Give the position of every Plasmodium parasite and every leukocyte.
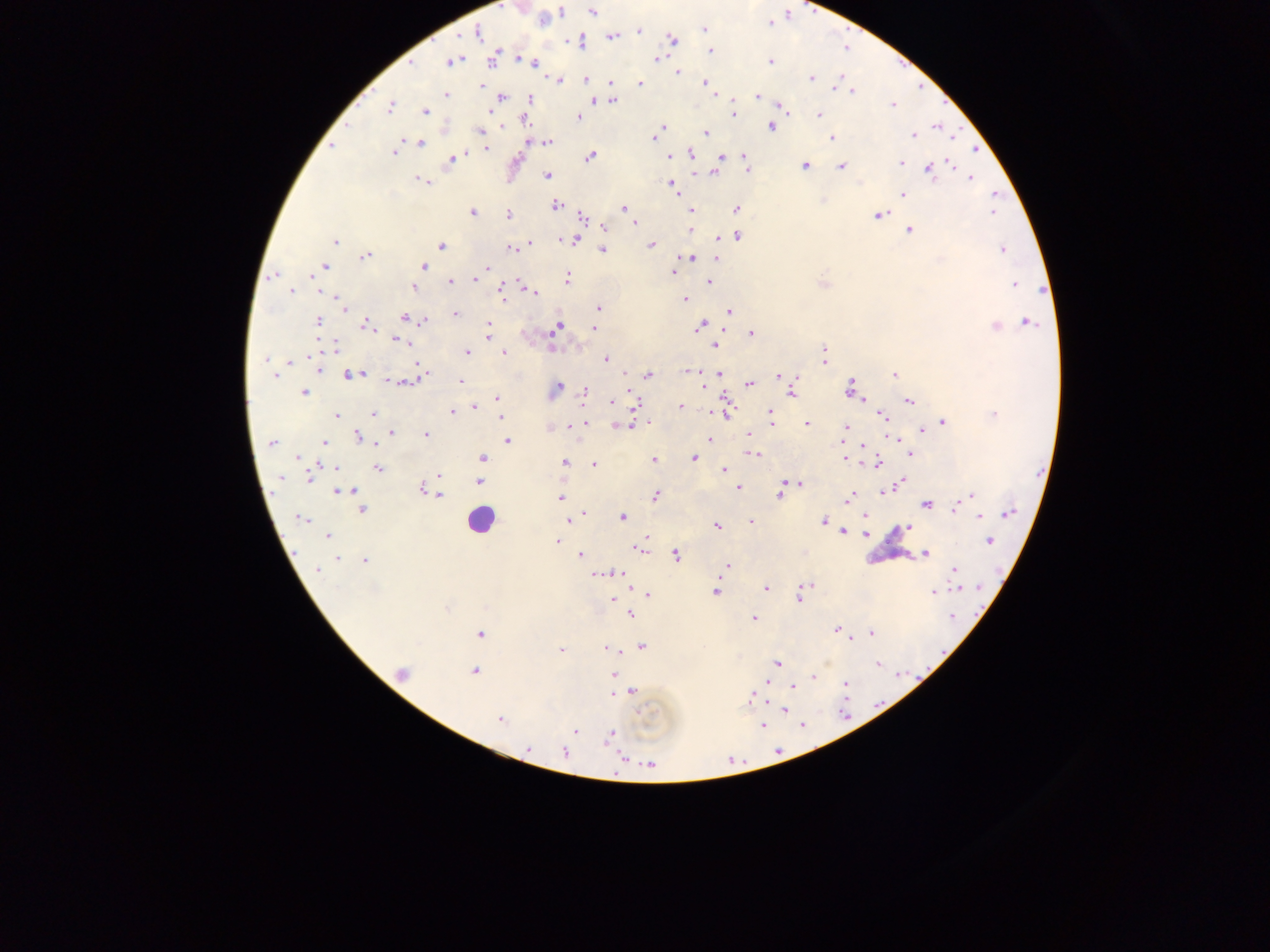
Approximate centers as x y in pixels.
Plasmodium parasites: 592 12; 543 19; 705 29; 639 31; 477 33; 612 37; 673 39; 579 42; 710 51; 492 59; 524 60; 657 60; 452 62; 532 62; 770 62; 677 73; 811 78; 586 79; 558 80; 611 82; 705 82; 640 83; 838 83; 481 85; 852 91; 446 95; 757 96; 502 97; 531 98; 594 101; 613 101; 892 105; 390 106; 783 108; 425 111; 734 112; 820 114; 579 117; 524 121; 770 127; 661 129; 481 130; 706 133; 914 135; 656 137; 832 138; 547 142; 420 143; 332 146; 485 148; 977 150; 394 153; 691 153; 455 155; 589 156; 669 156; 744 156; 720 157; 452 159; 900 162; 952 164; 804 166; 841 167; 748 170; 929 171; 714 173; 547 176; 972 178; 423 181; 672 184; 995 194; 903 195; 556 205; 624 208; 737 208; 691 211; 992 212; 473 213; 508 215; 879 215; 583 217; 634 223; 604 228; 691 230; 909 230; 577 236; 737 236; 571 239; 335 241; 529 244; 651 245; 441 246; 511 248; 602 250; 1002 250; 365 256; 690 258; 716 259; 423 266; 324 267; 487 269; 672 272; 272 276; 567 278; 475 279; 450 283; 709 283; 1014 284; 414 288; 321 290; 291 291; 501 292; 532 292; 684 299; 339 301; 344 307; 599 308; 729 311; 455 314; 404 317; 318 321; 424 321; 1028 322; 365 325; 489 325; 699 326; 557 327; 995 327; 593 328; 752 334; 488 336; 398 340; 715 345; 335 346; 824 351; 468 352; 504 353; 605 359; 265 360; 289 362; 824 362; 320 370; 689 371; 361 374; 425 374; 648 374; 718 374; 895 374; 350 375; 274 376; 779 377; 796 378; 396 381; 407 382; 461 382; 750 384; 703 385; 558 386; 850 388; 586 391; 303 393; 791 393; 497 398; 861 398; 909 401; 611 402; 636 402; 680 406; 473 408; 452 412; 725 412; 374 413; 770 413; 994 414; 882 415; 336 416; 501 417; 585 422; 943 422; 772 423; 807 424; 570 425; 618 426; 626 427; 846 427; 922 431; 391 433; 425 434; 749 435; 358 436; 709 439; 892 439; 507 441; 324 442; 271 443; 863 444; 910 453; 754 454; 482 458; 694 458; 844 458; 298 459; 653 459; 565 462; 594 464; 875 464; 335 467; 378 468; 724 470; 309 475; 439 475; 481 475; 281 477; 479 481; 901 481; 785 482; 799 484; 423 489; 738 489; 781 489; 343 491; 430 491; 884 492; 656 494; 780 495; 971 495; 440 496; 560 498; 848 499; 926 505; 957 506; 363 510; 585 513; 1008 513; 864 515; 980 516; 622 517; 301 518; 570 519; 824 521; 751 522; 717 526; 907 528; 843 532; 865 533; 328 537; 558 541; 989 541; 638 547; 925 554; 580 555; 676 555; 336 559; 365 560; 728 565; 317 569; 955 569; 602 574; 620 574; 766 588; 958 588; 716 592; 933 592; 647 594; 799 597; 612 600; 447 609; 630 613; 952 617; 754 619; 837 630; 480 633; 871 633; 642 646; 606 649; 561 650; 777 663; 878 664; 474 672; 401 673; 613 675; 813 677; 846 684; 793 687; 632 692; 752 697; 784 710; 500 719; 764 725; 802 725; 575 730; 611 735; 528 748; 564 752; 620 758; 650 764.
Leukocytes: 481 521.

One field of view. Thick blood smear. Sample from Ghana. Photographed through a microscope with a mobile-phone camera. Image is 1270×952 pixels.